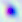
Micrograph. Captured at 400x magnification. Toxoplasma gondii is seen.